Give the extent of all Plasmodium ovale-infected red blood cells.
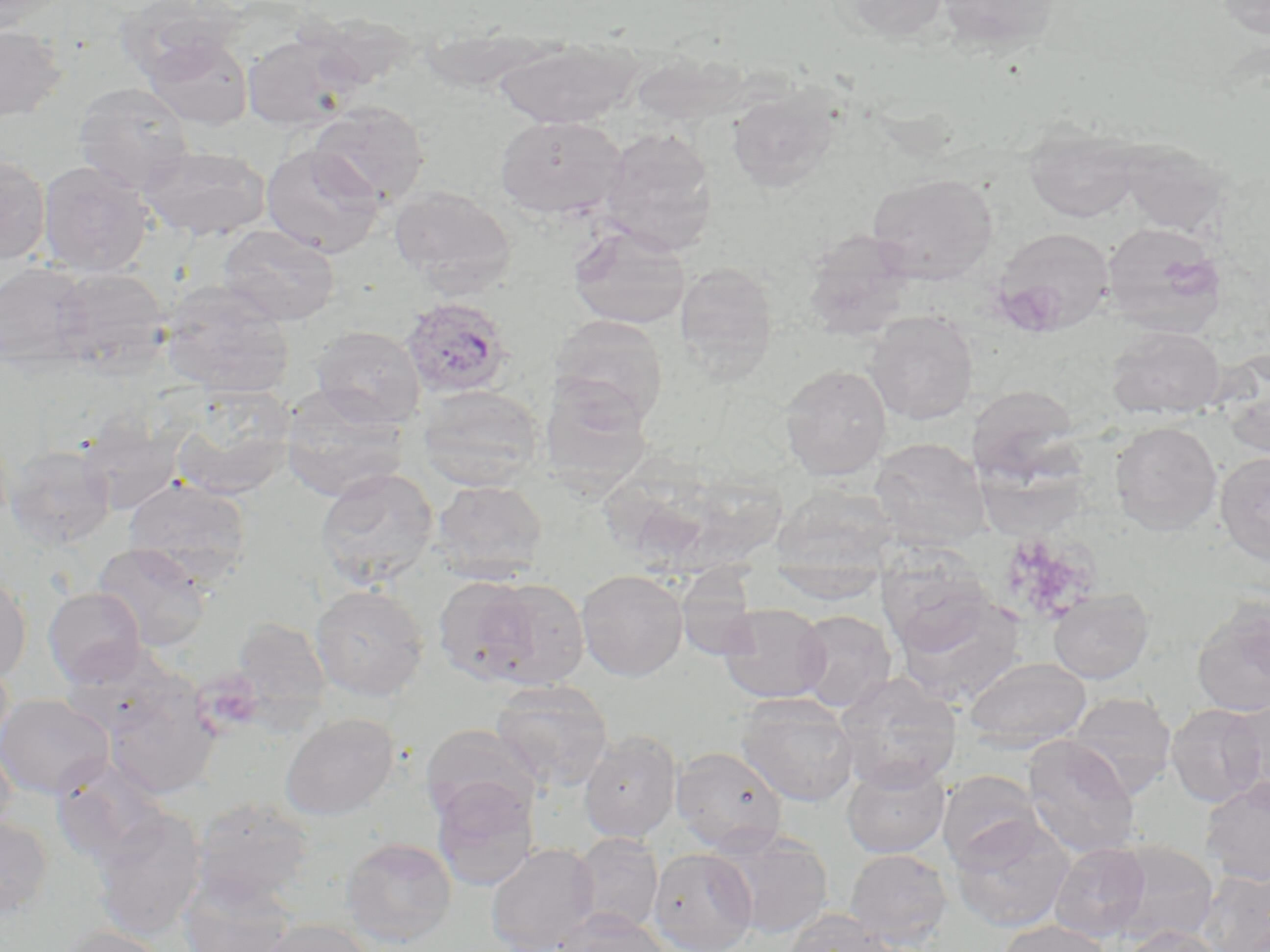

Approximate bounding boxes as named x1/y1/x2/y2 corners in pixels.
Plasmodium ovale-infected red blood cells: (x1=400, y1=295, x2=512, y2=399).

Uninfected red blood cell locations: (x1=0, y1=0, x2=68, y2=33), (x1=832, y1=0, x2=950, y2=43), (x1=934, y1=0, x2=1064, y2=53), (x1=1213, y1=0, x2=1270, y2=40), (x1=303, y1=11, x2=419, y2=90), (x1=0, y1=24, x2=68, y2=123), (x1=243, y1=31, x2=360, y2=132), (x1=143, y1=33, x2=254, y2=131), (x1=494, y1=35, x2=641, y2=128), (x1=628, y1=51, x2=723, y2=123), (x1=73, y1=82, x2=195, y2=195), (x1=727, y1=84, x2=842, y2=193), (x1=309, y1=102, x2=429, y2=208), (x1=495, y1=114, x2=625, y2=219), (x1=1024, y1=122, x2=1140, y2=223), (x1=600, y1=128, x2=718, y2=253), (x1=1118, y1=141, x2=1233, y2=239), (x1=139, y1=144, x2=271, y2=241), (x1=261, y1=144, x2=385, y2=258), (x1=0, y1=154, x2=51, y2=265), (x1=38, y1=161, x2=153, y2=276), (x1=867, y1=173, x2=998, y2=283), (x1=389, y1=185, x2=516, y2=291), (x1=1101, y1=221, x2=1228, y2=336), (x1=568, y1=222, x2=691, y2=329), (x1=217, y1=224, x2=340, y2=326), (x1=990, y1=228, x2=1114, y2=335), (x1=803, y1=230, x2=916, y2=340), (x1=674, y1=261, x2=779, y2=380), (x1=0, y1=263, x2=92, y2=366), (x1=51, y1=266, x2=171, y2=374), (x1=159, y1=280, x2=294, y2=398), (x1=865, y1=311, x2=978, y2=425), (x1=550, y1=314, x2=669, y2=426), (x1=311, y1=325, x2=425, y2=427), (x1=1107, y1=326, x2=1226, y2=419), (x1=779, y1=364, x2=892, y2=482), (x1=1221, y1=364, x2=1270, y2=458), (x1=967, y1=384, x2=1080, y2=484), (x1=169, y1=385, x2=297, y2=500), (x1=279, y1=385, x2=410, y2=502), (x1=417, y1=385, x2=546, y2=491), (x1=76, y1=411, x2=188, y2=515), (x1=1110, y1=422, x2=1222, y2=535), (x1=869, y1=438, x2=991, y2=547), (x1=4, y1=444, x2=116, y2=550), (x1=1215, y1=451, x2=1270, y2=565), (x1=315, y1=467, x2=439, y2=589), (x1=123, y1=478, x2=252, y2=588), (x1=432, y1=480, x2=549, y2=582), (x1=772, y1=484, x2=899, y2=571), (x1=92, y1=543, x2=212, y2=652), (x1=875, y1=551, x2=996, y2=657), (x1=769, y1=569, x2=886, y2=604), (x1=576, y1=570, x2=689, y2=681), (x1=673, y1=572, x2=764, y2=660), (x1=0, y1=574, x2=32, y2=684), (x1=433, y1=575, x2=541, y2=686), (x1=471, y1=577, x2=590, y2=689), (x1=309, y1=584, x2=429, y2=701), (x1=43, y1=587, x2=146, y2=687), (x1=1048, y1=587, x2=1154, y2=684), (x1=894, y1=592, x2=1026, y2=707), (x1=1192, y1=598, x2=1270, y2=717), (x1=718, y1=603, x2=831, y2=703), (x1=794, y1=610, x2=896, y2=711), (x1=231, y1=617, x2=332, y2=722), (x1=59, y1=646, x2=188, y2=741), (x1=0, y1=654, x2=14, y2=760), (x1=962, y1=657, x2=1092, y2=752), (x1=834, y1=672, x2=962, y2=792), (x1=490, y1=679, x2=614, y2=790), (x1=102, y1=685, x2=221, y2=799), (x1=1066, y1=692, x2=1177, y2=798), (x1=736, y1=693, x2=860, y2=807), (x1=0, y1=694, x2=114, y2=799), (x1=1221, y1=700, x2=1270, y2=803), (x1=1166, y1=703, x2=1268, y2=807), (x1=280, y1=712, x2=400, y2=821), (x1=420, y1=724, x2=540, y2=825), (x1=579, y1=730, x2=681, y2=842), (x1=1023, y1=736, x2=1141, y2=860), (x1=0, y1=739, x2=18, y2=844), (x1=670, y1=746, x2=788, y2=854), (x1=49, y1=757, x2=171, y2=868), (x1=842, y1=758, x2=950, y2=858), (x1=938, y1=770, x2=1042, y2=867), (x1=1200, y1=776, x2=1270, y2=886), (x1=431, y1=778, x2=539, y2=891), (x1=189, y1=796, x2=316, y2=907), (x1=89, y1=807, x2=207, y2=940), (x1=948, y1=814, x2=1074, y2=932), (x1=0, y1=816, x2=53, y2=921), (x1=711, y1=829, x2=835, y2=938), (x1=570, y1=833, x2=664, y2=933), (x1=340, y1=836, x2=458, y2=948), (x1=1106, y1=841, x2=1219, y2=945), (x1=485, y1=842, x2=599, y2=952), (x1=1050, y1=842, x2=1151, y2=941), (x1=648, y1=848, x2=758, y2=952), (x1=845, y1=848, x2=952, y2=947), (x1=1200, y1=870, x2=1270, y2=952), (x1=177, y1=874, x2=296, y2=952), (x1=553, y1=909, x2=672, y2=952), (x1=781, y1=909, x2=900, y2=952), (x1=258, y1=919, x2=375, y2=952), (x1=1000, y1=919, x2=1112, y2=952), (x1=52, y1=925, x2=172, y2=952), (x1=1119, y1=925, x2=1224, y2=952). Slide-level diagnosis: Plasmodium ovale. May-Grünwald-Giemsa-stained preparation. Light microscopy. One field of a larger specimen. Captured at 1000x magnification. Image is 1270×952 pixels. Thin blood smear.